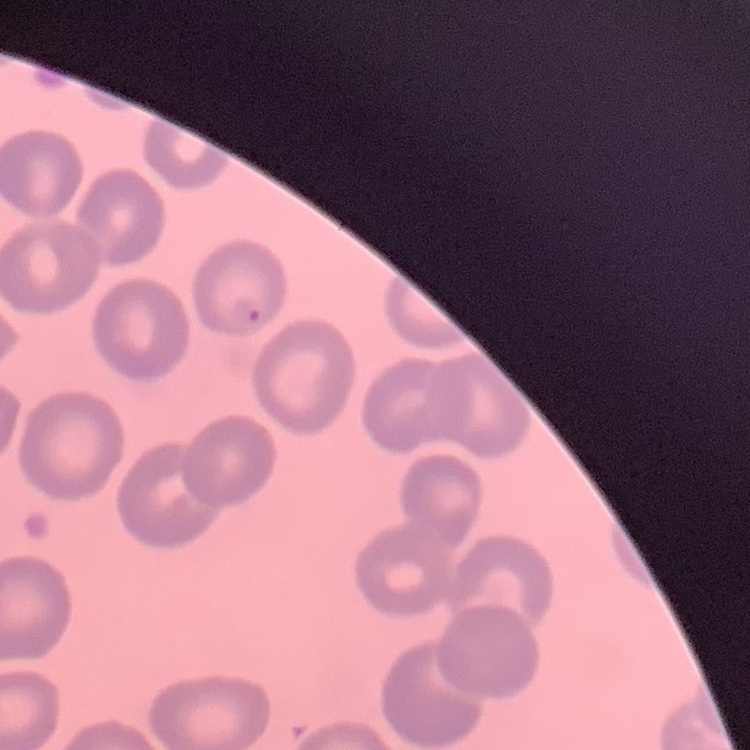
Summary:
  - Red blood cell morphology: no rouleaux formation
  - Image type: square crop of a larger photomicrograph
  - Preparation: thin blood smear
  - Stain: Field's or Giemsa